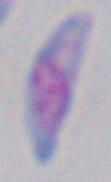

modality = photomicrograph
identification = Toxoplasma gondii
magnification = 1000x